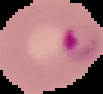
Summary:
  - Malaria status: parasitized
  - Image type: segmented cell region on a black background
  - Preparation: thin blood smear
  - Image size: 103×94 pixels